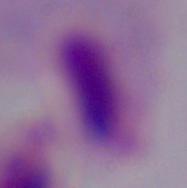

Captured at 1000x magnification. A trichomonad is shown. Micrograph.